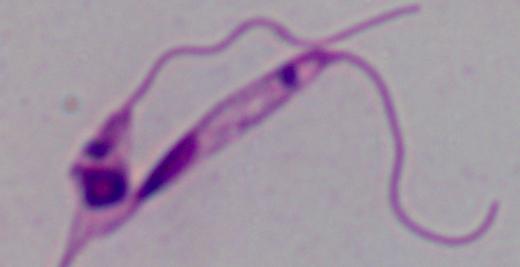 A Leishmania parasite is shown. Photomicrograph. 1000x magnification.